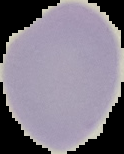

Summary:
  - Preparation: thin blood smear
  - Malaria status: uninfected
  - Image type: segmented cell region on a black background
  - Image size: 124×154 pixels